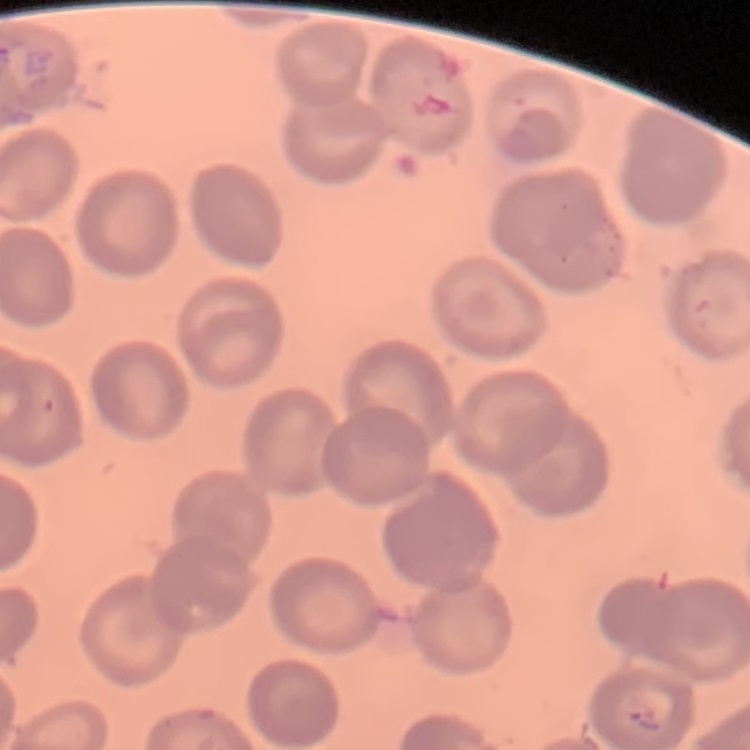
Summary:
  - Red blood cell morphology: no rouleaux formation
  - Image type: one tile cut from a larger photomicrograph
  - Stain: Field's or Giemsa
  - Preparation: thin blood smear